Report the malaria status of this cell.
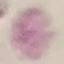

Uninfected.

Summary:
  - Preparation: thin blood smear
  - Capture: smartphone through the microscope eyepiece
  - Image type: automatically extracted cell patch, resized to 64 × 64 pixels
  - Stain: Giemsa